Locate every Plasmodium vivax-infected red blood cell.
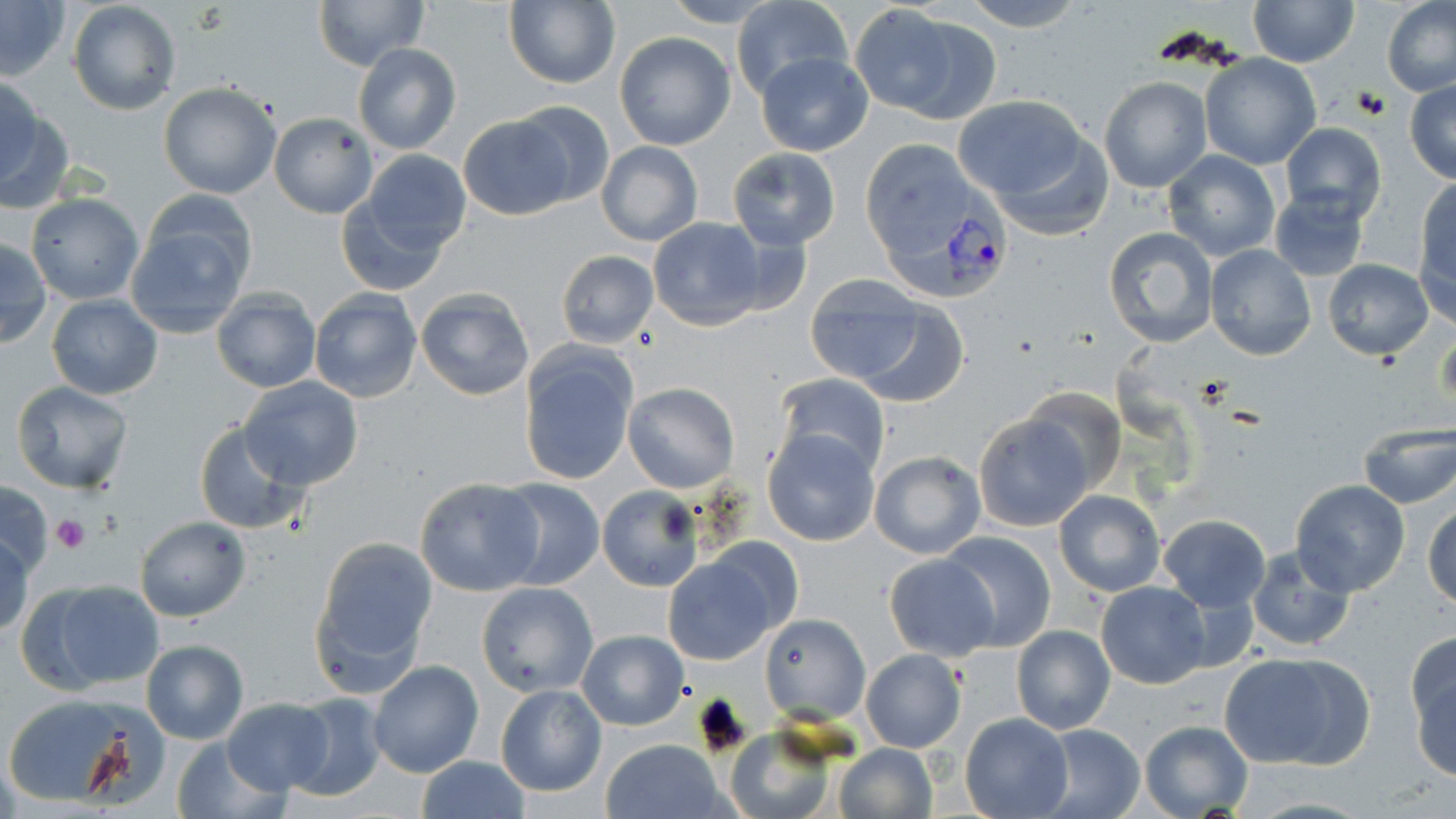

Approximate bounding boxes as (x1, y1, x2, y2) in pixels.
Plasmodium vivax-infected red blood cells: (879, 173, 1012, 304).

Uninfected red blood cell locations: (314, 0, 426, 70), (660, 0, 784, 27), (957, 0, 1088, 32), (67, 1, 181, 116), (502, 1, 621, 88), (732, 1, 854, 101), (1248, 1, 1359, 67), (1382, 1, 1456, 98), (0, 2, 71, 81), (865, 7, 1002, 123), (614, 31, 737, 150), (353, 43, 460, 154), (755, 51, 873, 156), (1201, 53, 1321, 169), (0, 73, 45, 191), (1099, 76, 1212, 191), (1405, 78, 1456, 183), (158, 83, 283, 199), (953, 95, 1090, 208), (510, 99, 618, 210), (0, 102, 72, 216), (268, 112, 378, 219), (460, 115, 573, 220), (1279, 123, 1386, 224), (978, 124, 1117, 244), (596, 140, 703, 247), (859, 141, 984, 262), (727, 147, 841, 250), (356, 148, 472, 254), (1161, 149, 1281, 262), (1413, 176, 1456, 297), (142, 188, 258, 286), (1269, 190, 1369, 281), (26, 194, 143, 305), (337, 196, 455, 296), (124, 217, 253, 339), (647, 218, 767, 331), (701, 224, 812, 323), (1100, 226, 1218, 348), (0, 238, 50, 348), (1205, 244, 1316, 360), (555, 250, 659, 347), (1322, 258, 1434, 360), (803, 274, 927, 386), (212, 287, 321, 394), (414, 287, 537, 402), (309, 289, 423, 404), (46, 294, 162, 400), (853, 300, 969, 410), (518, 347, 637, 488), (773, 375, 890, 481), (238, 377, 364, 490), (11, 382, 134, 495), (623, 382, 739, 493), (1021, 384, 1123, 493), (972, 413, 1093, 531), (192, 422, 305, 536), (1355, 425, 1456, 510), (762, 428, 881, 547), (869, 450, 985, 559), (414, 477, 544, 596), (491, 478, 605, 592), (0, 481, 52, 577), (1291, 481, 1409, 596), (597, 486, 702, 592), (1054, 490, 1166, 596), (1424, 500, 1456, 610), (1158, 513, 1270, 613), (135, 517, 251, 621), (939, 530, 1056, 652), (0, 531, 31, 638), (311, 535, 438, 690), (1243, 545, 1355, 652), (883, 554, 998, 661), (662, 555, 780, 664), (25, 578, 166, 692), (1097, 581, 1210, 689), (477, 582, 598, 697), (761, 614, 869, 724), (1011, 625, 1115, 734), (578, 630, 688, 731), (1406, 638, 1456, 775), (142, 639, 248, 743), (525, 643, 680, 760), (862, 649, 966, 752), (1220, 649, 1374, 771), (368, 660, 484, 779), (496, 683, 606, 798), (283, 691, 389, 802), (1, 693, 156, 806), (221, 697, 334, 794), (959, 713, 1072, 819), (1137, 720, 1253, 819), (1032, 723, 1148, 819), (727, 728, 837, 819), (170, 735, 287, 819), (601, 738, 726, 818), (834, 742, 939, 819), (416, 756, 530, 819). Platelet locations: (50, 512, 90, 555). Slide-level diagnosis: Plasmodium vivax. Single field of view. 1000x magnification. Image is 1456×819 pixels. Light microscopy. Thin blood film. May-Grünwald-Giemsa-stained preparation.